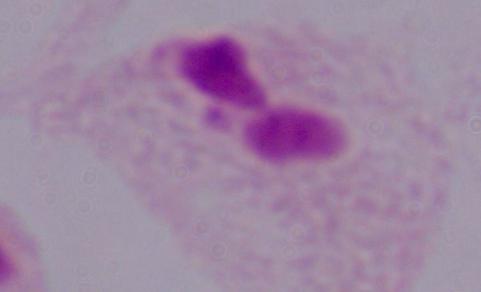
Summary:
  - Identification: trichomonad
  - Magnification: 1000x
  - Modality: micrograph